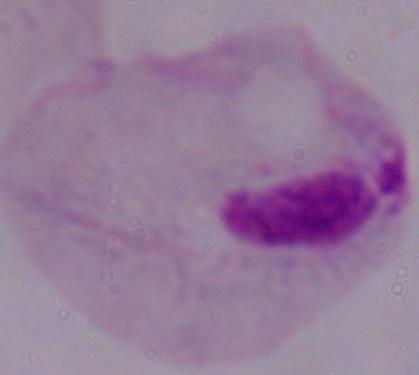

Micrograph. A trichomonad is seen. Captured at 1000x magnification.